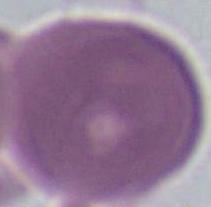
A red blood cell is shown. 1000x magnification. Photomicrograph.